State which cell type is depicted.
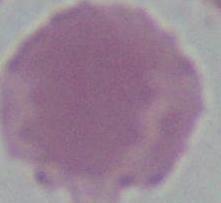

This is an erythrocyte.

Captured at 1000x magnification. Micrograph.